State which parasite is depicted.
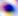
This is Toxoplasma gondii.

Summary:
  - Magnification: 400x
  - Modality: micrograph